Outline each Plasmodium ovale-infected red blood cell.
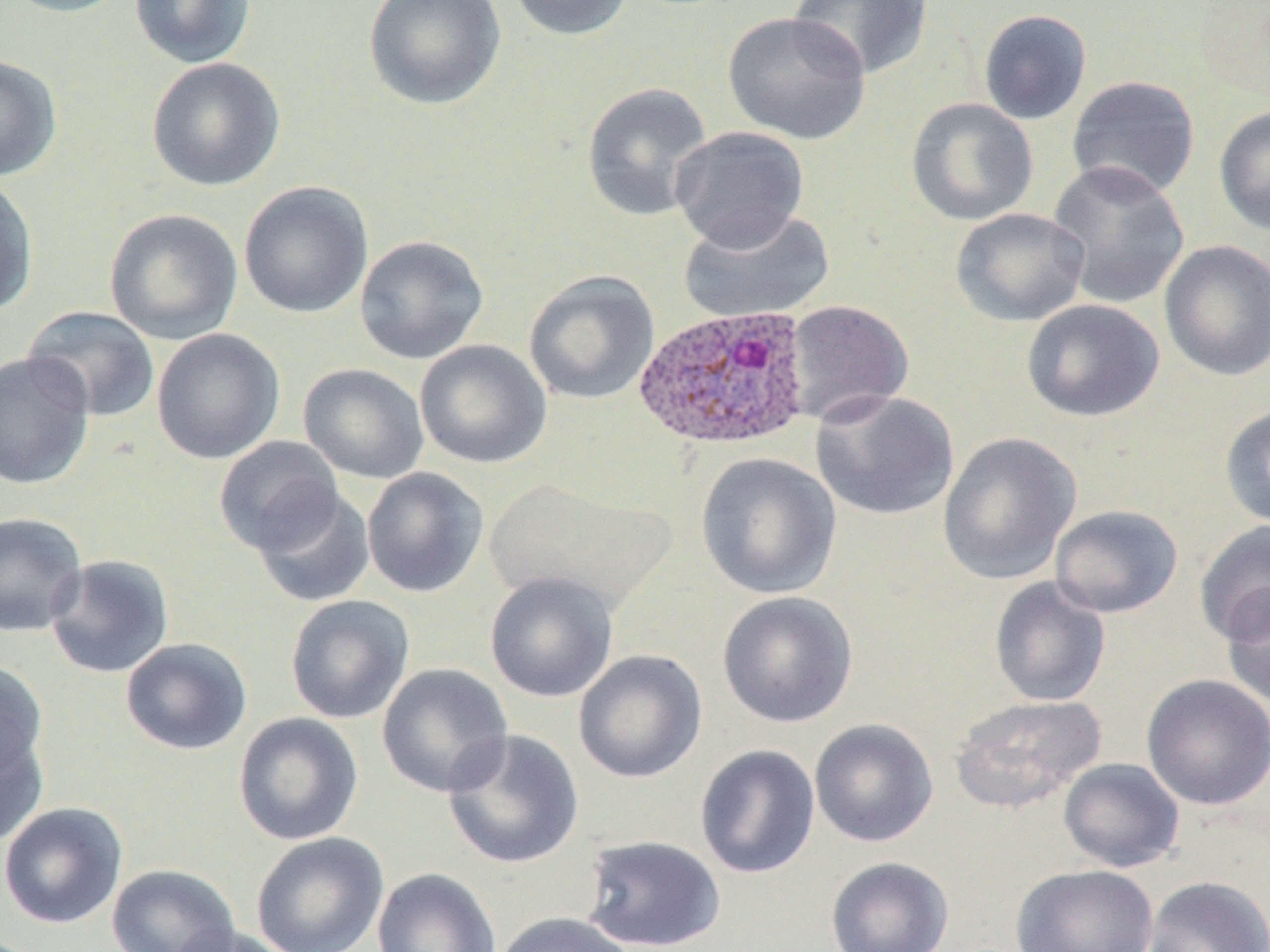
Approximate bounding boxes as [x1, y1, x2, y2] in pixels.
Plasmodium ovale-infected red blood cells: [634, 305, 813, 451].

Uninfected red blood cell locations: [0, 0, 133, 18], [129, 0, 257, 69], [363, 0, 505, 110], [506, 0, 633, 41], [789, 0, 934, 80], [1192, 0, 1270, 105], [978, 9, 1092, 125], [722, 10, 871, 145], [0, 55, 62, 181], [146, 56, 286, 192], [1067, 75, 1201, 200], [581, 82, 714, 222], [906, 97, 1038, 226], [1213, 105, 1270, 235], [668, 125, 811, 252], [1047, 160, 1190, 310], [0, 176, 39, 317], [238, 180, 373, 318], [678, 207, 835, 324], [951, 207, 1091, 327], [103, 208, 243, 345], [354, 234, 489, 365], [1159, 240, 1270, 382], [523, 270, 660, 405], [1021, 299, 1165, 422], [783, 300, 914, 426], [22, 306, 160, 423], [151, 328, 285, 464], [415, 340, 552, 469], [0, 351, 95, 490], [297, 363, 430, 484], [811, 389, 960, 521], [1219, 403, 1270, 530], [937, 432, 1081, 586], [213, 435, 345, 556], [695, 452, 842, 599], [362, 467, 490, 597], [485, 477, 671, 613], [251, 487, 376, 608], [1049, 504, 1183, 618], [0, 511, 88, 637], [1194, 519, 1270, 647], [44, 554, 175, 678], [484, 571, 618, 703], [988, 577, 1111, 707], [1220, 584, 1270, 710], [717, 591, 858, 728], [284, 594, 415, 724], [120, 637, 253, 756], [573, 649, 707, 783], [0, 661, 49, 782], [376, 663, 514, 797], [1141, 674, 1270, 810], [949, 693, 1107, 814], [233, 712, 364, 847], [809, 718, 939, 847], [442, 728, 585, 869], [0, 729, 48, 847], [694, 744, 821, 879], [1058, 757, 1185, 873], [0, 801, 128, 929], [251, 832, 389, 952], [580, 834, 728, 951], [825, 856, 954, 952], [107, 863, 240, 952], [1011, 864, 1159, 952], [372, 868, 501, 952], [1143, 876, 1269, 952], [492, 911, 637, 952], [168, 925, 297, 952]. Slide-level diagnosis: Plasmodium ovale. May-Grünwald-Giemsa-stained preparation. 1000x magnification. Light microscopy. Image is 1270×952 pixels. Single field of view. Thin blood film.